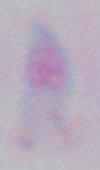 Toxoplasma gondii is seen. Captured at 1000x magnification. Photomicrograph.